Draw a bounding box around every leukocyte (white blood cell).
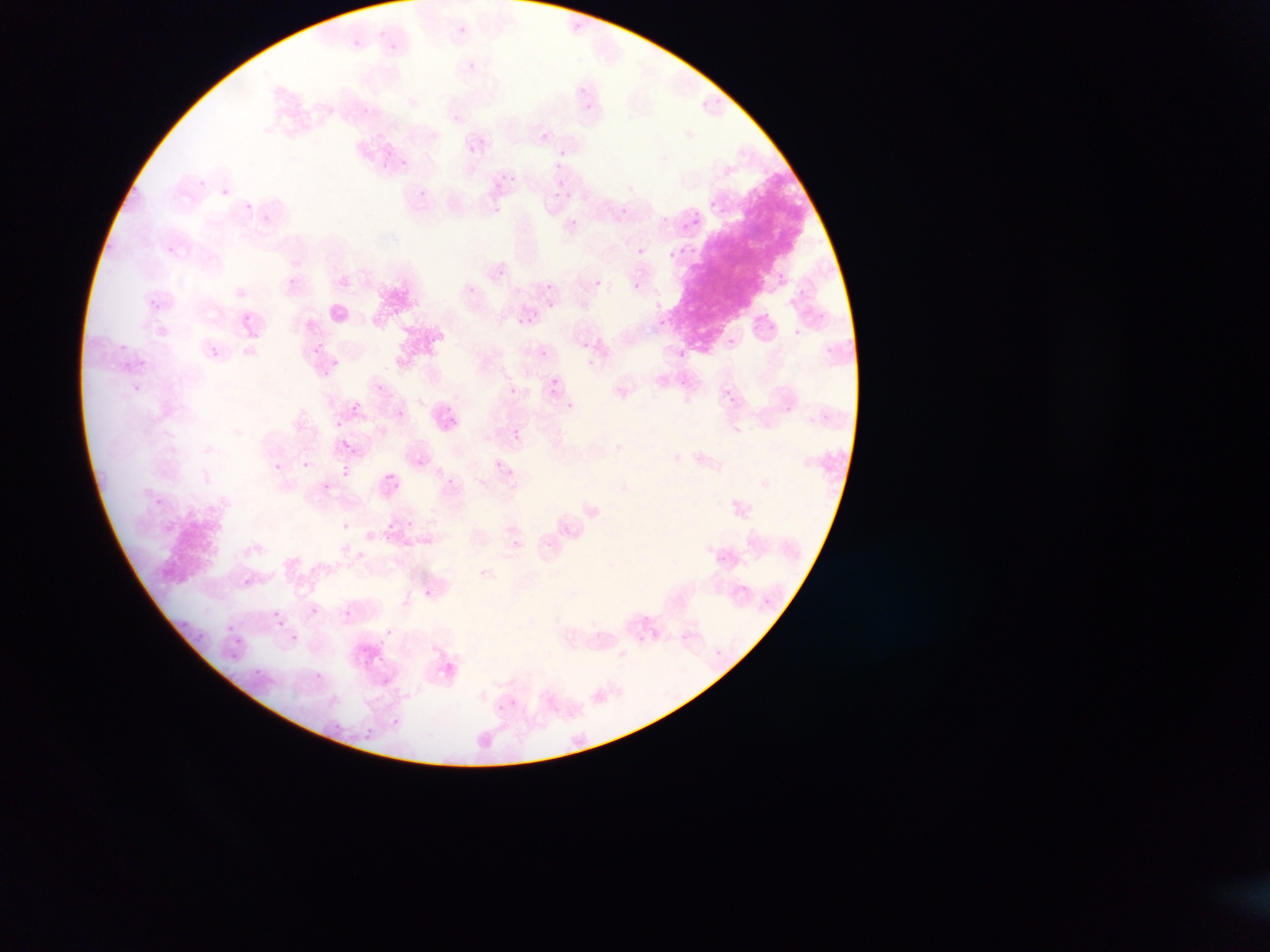
No leukocytes observed.

{
  "image_size": "1270×952 pixels",
  "field_of_view": "single",
  "capture": "mobile-phone photograph through a microscope",
  "country": "Ghana",
  "preparation": "thin blood smear",
  "malaria_parasite_locations": "approximate bounding boxes as left top right bottom in pixels: 199 179 207 187; 558 182 566 188; 692 220 701 225; 632 248 647 255; 778 273 786 280; 634 282 642 289; 154 304 162 310; 531 311 540 319; 764 311 770 319; 659 320 667 325; 726 337 737 345; 120 345 129 350; 311 349 322 355; 680 349 691 358; 212 351 221 357; 331 360 340 367; 551 379 559 385; 725 389 733 394; 567 401 575 407; 513 435 521 439; 275 464 281 472; 342 466 350 469; 323 484 331 490; 406 520 415 526; 343 522 352 528; 514 538 522 545; 311 606 319 612; 271 612 279 616; 644 614 648 622; 226 627 234 632; 386 629 392 637; 235 638 243 646; 716 649 721 657; 230 652 234 660; 379 655 385 663; 315 673 324 680; 392 718 400 723 | approximate x y pixel centers of objects too small to bound: 579 25; 463 29; 382 34; 356 43; 393 47; 472 66; 583 88; 589 106; 365 110; 454 117; 545 136; 480 140; 471 150; 563 152; 404 162; 386 164; 558 166; 504 177; 512 178; 226 192; 422 193; 557 193; 568 195; 712 204; 249 205; 498 209; 625 209; 722 210; 697 214; 265 218; 576 222; 686 225; 693 249; 170 250; 682 250; 673 254; 291 281; 599 283; 549 285; 549 299; 152 302; 550 305; 659 305; 248 319; 520 320; 530 321; 757 327; 773 327; 797 331; 257 336; 321 344; 587 345; 215 349; 829 350; 544 354; 143 362; 592 363; 327 374; 684 382; 381 388; 138 389; 514 391; 552 391; 733 400; 357 405; 355 409; 789 410; 402 414; 339 423; 516 430; 347 446; 499 463; 305 465; 511 472; 345 475; 386 477; 392 477; 398 485; 391 526; 549 545; 718 559; 724 559; 484 572; 247 581; 745 587; 428 592; 767 603; 347 613; 185 624; 281 624; 295 638; 641 639; 199 640; 259 672; 512 702; 500 708; 337 727"
}